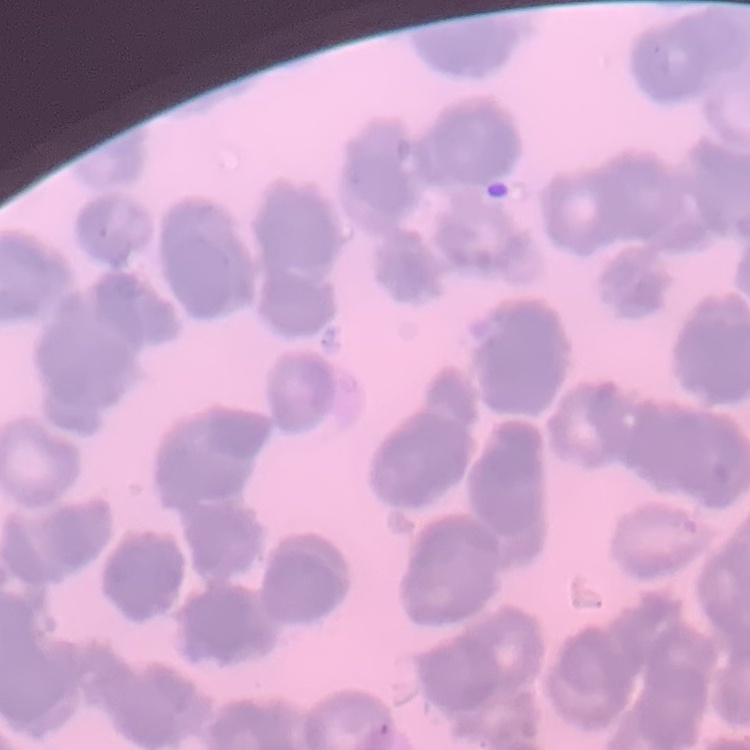

Summary:
  - Red blood cell morphology: rouleaux formation
  - Stain: Field's or Giemsa
  - Image type: square crop of a larger photomicrograph
  - Preparation: thin blood film